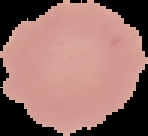
Image is 148×136 pixels. Cell region segmented out of the field of view; the surrounding area is masked to black. From a thin blood smear. Malaria status: uninfected.